Report the malaria status.
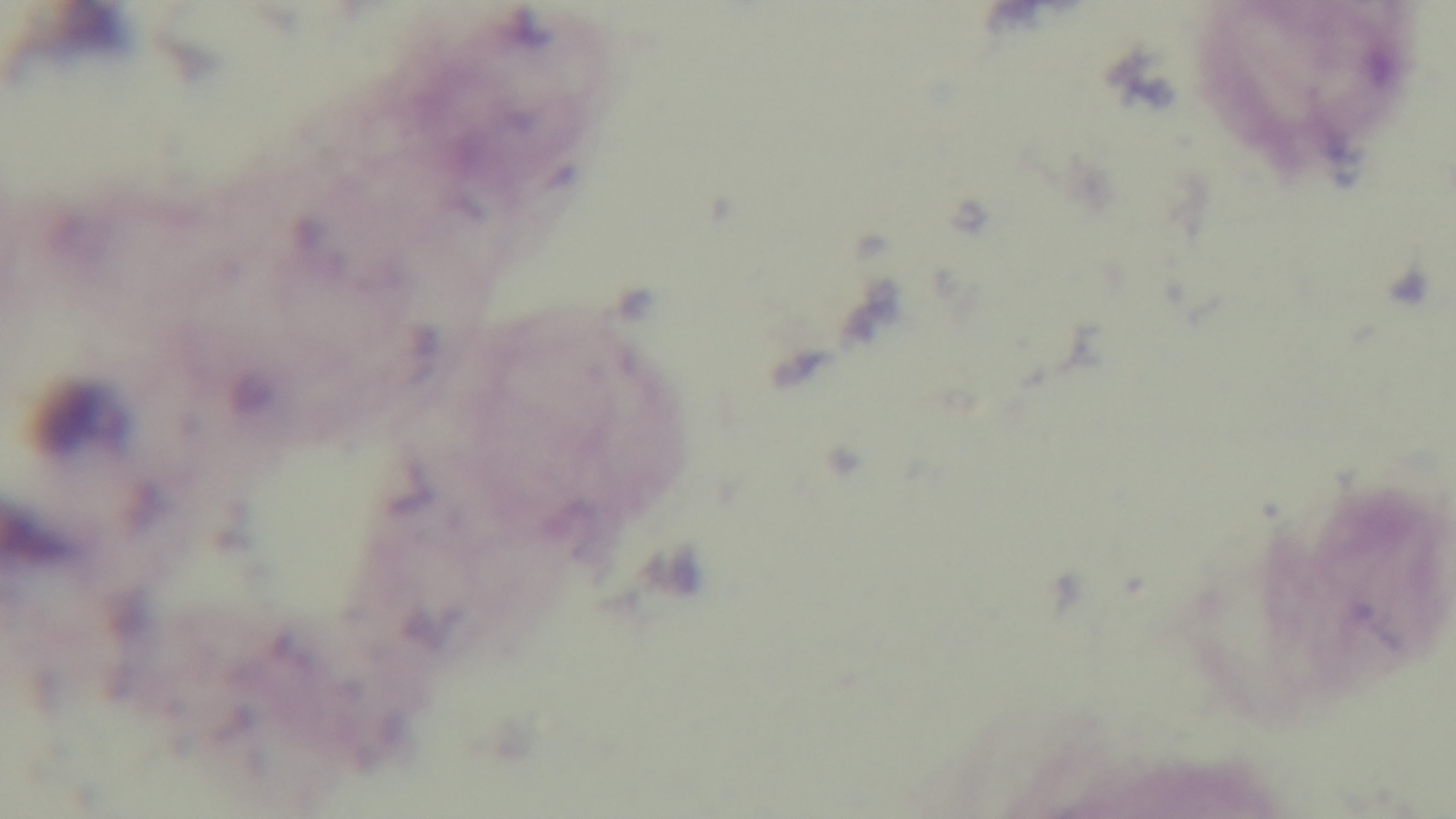
Uninfected.

Captured with a mounted 4K digital camera. Giemsa stain. Photomicrograph. Single field of view. Preparation: thick smear. 100x oil-immersion objective.